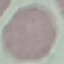

result = no malaria parasites seen
capture = smartphone through the microscope eyepiece
preparation = thin blood smear
stain = Giemsa
image type = cell patch, automatically extracted from a larger field of view and resized to 64 × 64 pixels